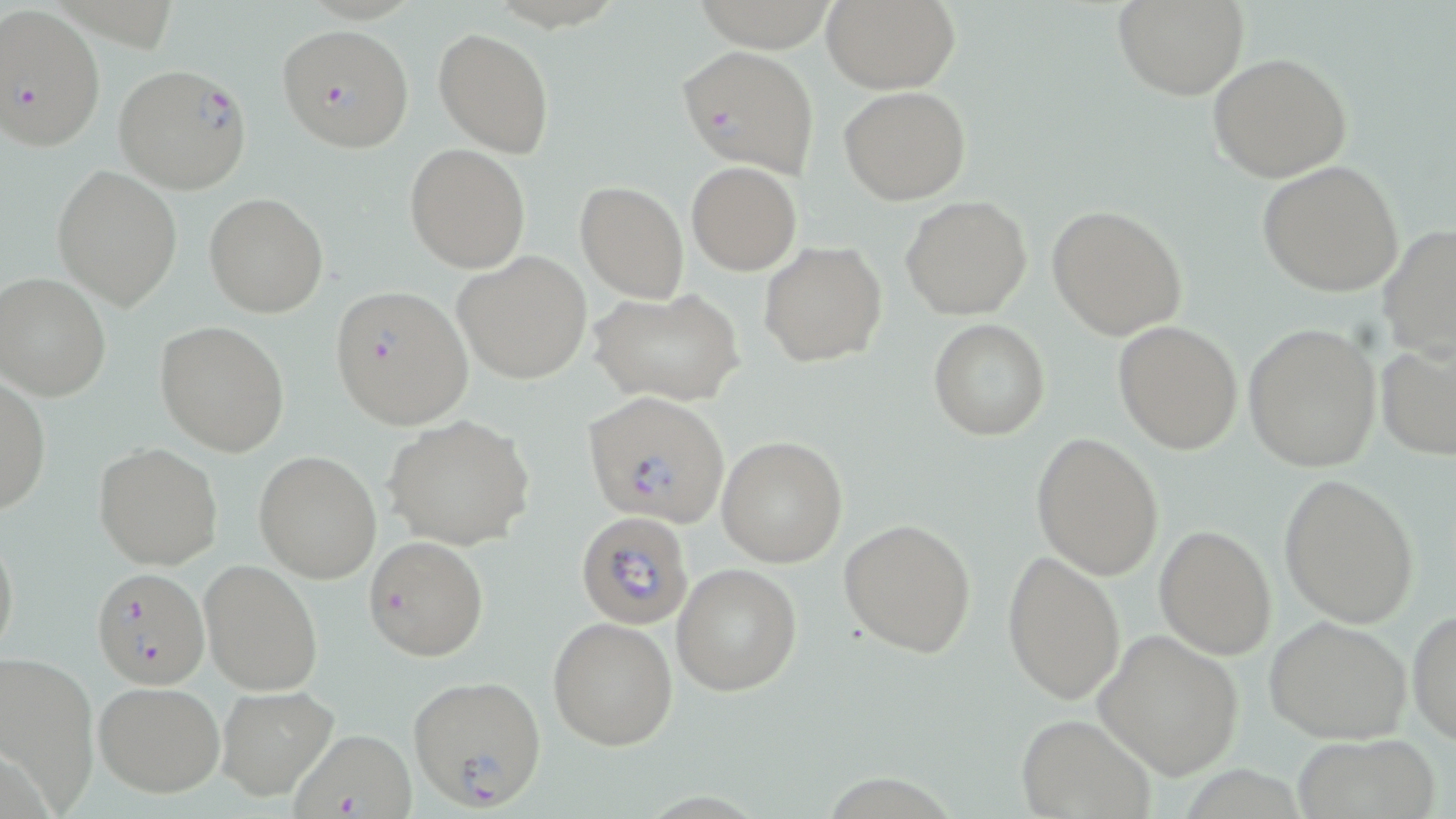

Summary:
  - Coordinate format: approximate bounding boxes as (x1, y1, x2, y2) in pixels
  - Uninfected red blood cell locations: (821, 0, 960, 91), (1115, 1, 1247, 100), (434, 27, 556, 158), (1207, 52, 1353, 183), (838, 86, 971, 205), (405, 144, 530, 272), (1257, 160, 1404, 297), (687, 161, 802, 274), (52, 165, 183, 308), (575, 181, 689, 302), (204, 193, 328, 317), (900, 195, 1032, 320), (1046, 204, 1187, 339), (1379, 224, 1456, 361), (759, 241, 888, 367), (452, 251, 592, 383), (0, 272, 111, 401), (590, 287, 745, 407), (928, 320, 1050, 441), (154, 321, 291, 455), (1113, 321, 1243, 454), (1244, 324, 1383, 472), (1376, 335, 1456, 459), (1, 377, 51, 518), (383, 415, 537, 550), (1031, 433, 1164, 581), (718, 436, 847, 566), (94, 443, 223, 570), (254, 450, 382, 583), (1278, 473, 1421, 628), (839, 519, 977, 657), (1, 525, 19, 663), (1154, 525, 1277, 659), (1003, 551, 1126, 706), (199, 558, 324, 698), (670, 563, 803, 697), (1408, 607, 1456, 747), (1264, 615, 1411, 745), (548, 616, 678, 749), (1095, 629, 1245, 780), (0, 652, 100, 812), (94, 681, 224, 797), (215, 685, 340, 803), (1013, 712, 1156, 819), (1291, 732, 1441, 819)
  - Plasmodium falciparum-infected red blood cell locations: (0, 4, 106, 151), (277, 22, 413, 154), (676, 45, 820, 178), (112, 63, 252, 195), (329, 284, 474, 429), (581, 391, 730, 528), (575, 509, 694, 630), (363, 536, 488, 660), (91, 565, 211, 689), (407, 674, 548, 809), (287, 729, 419, 819)
  - Slide-level diagnosis: Plasmodium falciparum
  - Stain: May-Grünwald-Giemsa
  - Field of view: single
  - Image size: 1456×819 pixels
  - Magnification: 1000x
  - Modality: optical microscopy
  - Preparation: thin blood film